Classify this cell by malaria status.
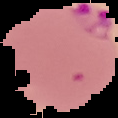

Parasitized.

image type = segmented cell region with the area outside set to black
preparation = thin blood smear
image size = 118×118 pixels